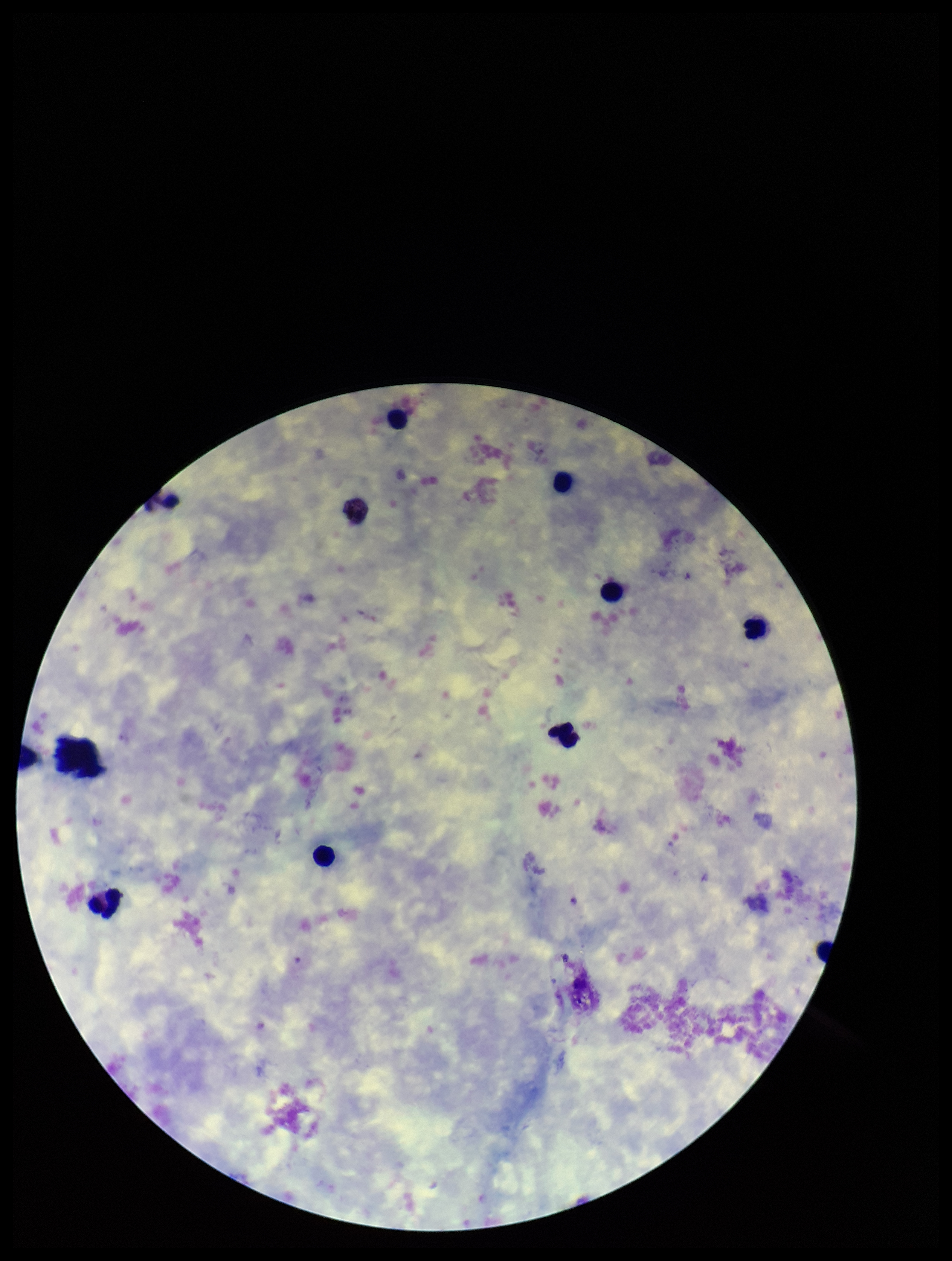
Summary:
  - Patient malaria status: infected
  - Parasite count: 0
  - Image size: 952×1261 pixels
  - Capture: smartphone photograph through the microscope eyepiece
  - Stain: Giemsa
  - Field of view: one from this slide
  - Plasmodium parasites: none seen
  - Leukocyte count: 9
  - Preparation: thick smear
  - Species reported for this patient: Plasmodium vivax